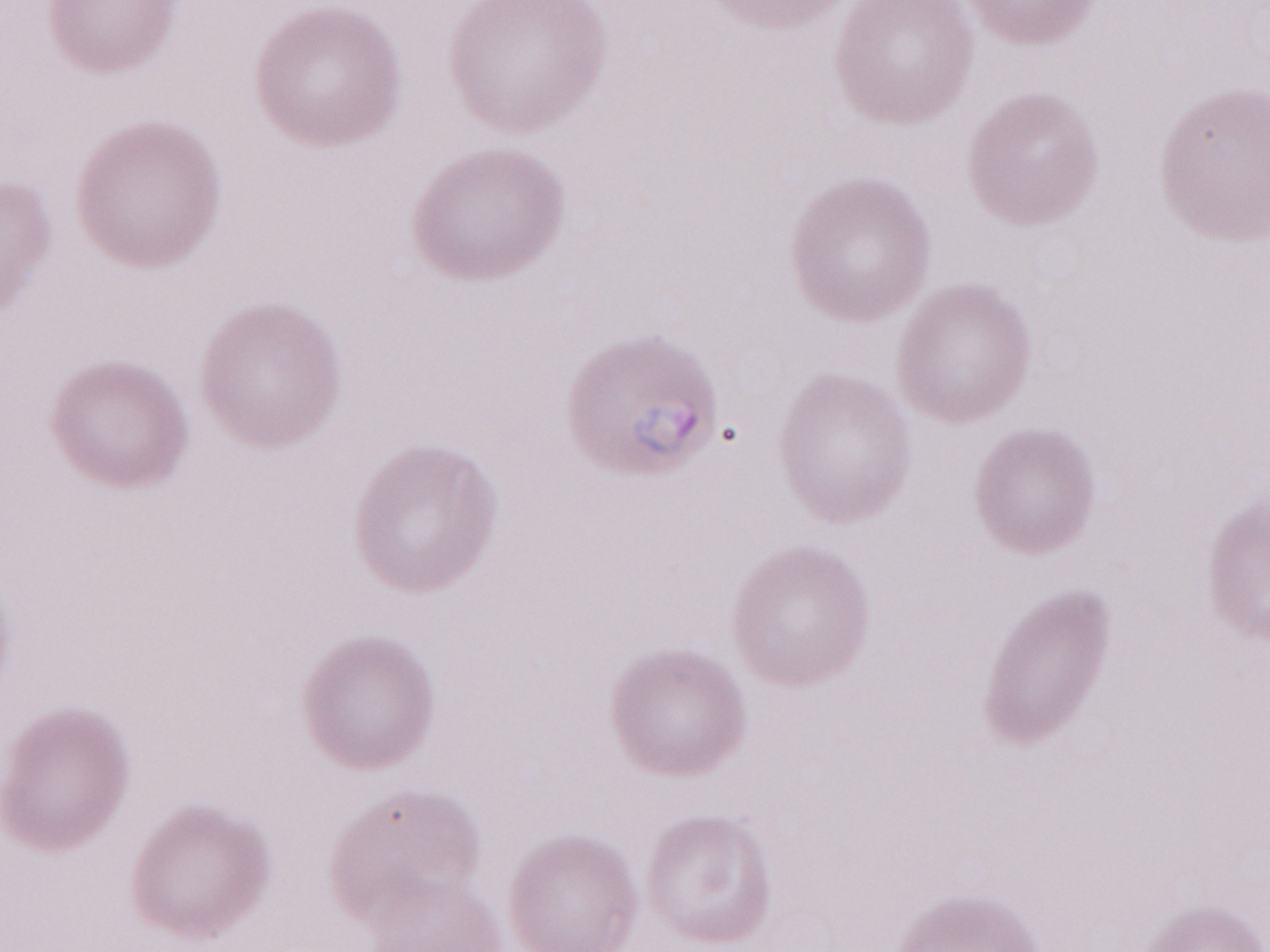
Patient diagnosis: malaria infection. Thin blood smear. Olympus BX43 microscope and DP73 digital camera. Image is 1270×952 pixels. Single field of view. Magnification: 1,000x. May-Grünwald-Giemsa (MGG) stain.